State the preparation type.
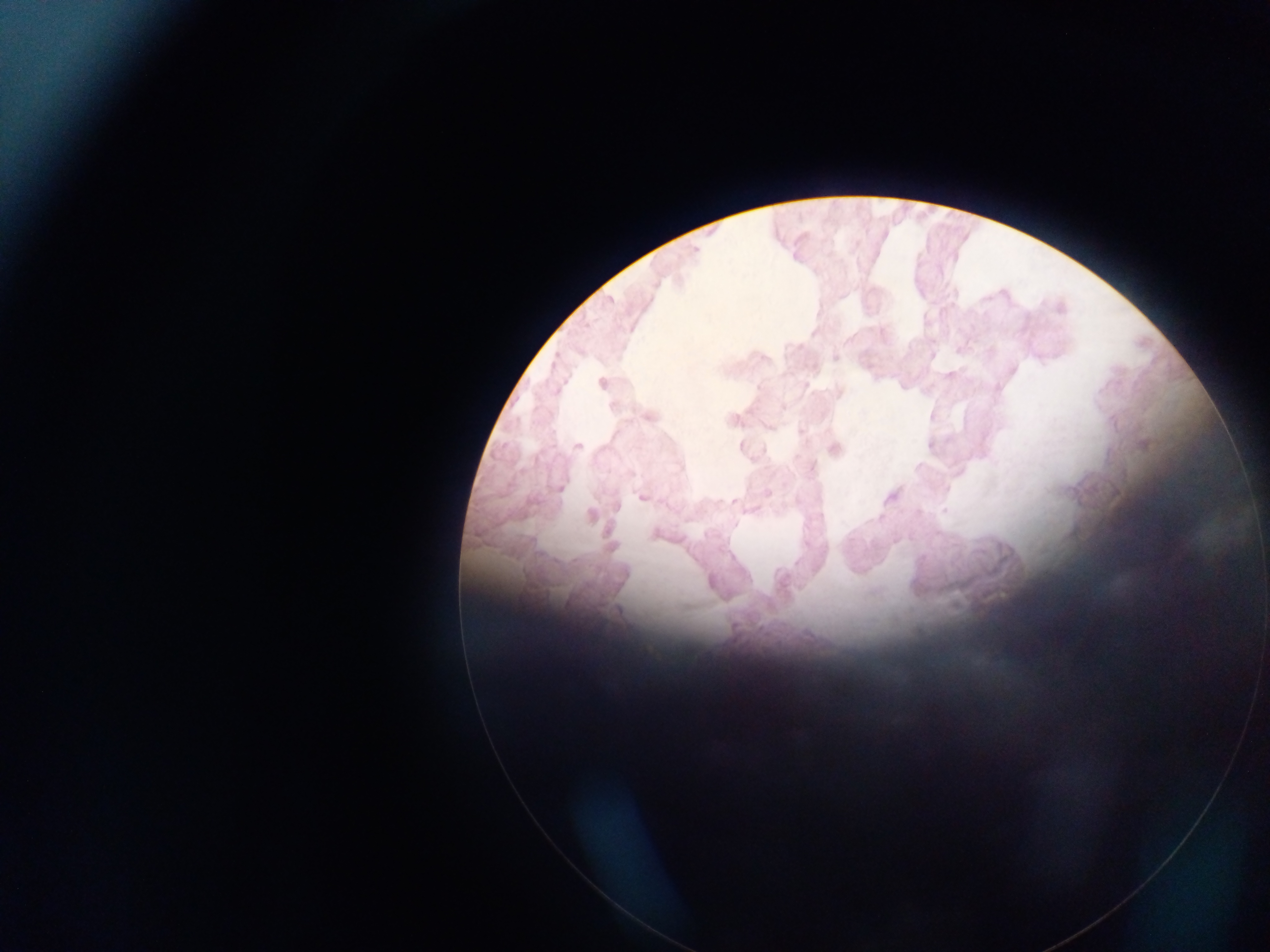
Thick blood smear.

image size = 1270×952 pixels
malaria parasite locations = approximate centers as x y in pixels: 697 247; 834 359; 578 445; 944 511
field of view = single
capture = mobile-phone photograph through a microscope
country = Ghana